Describe the morphology of the red blood cells.
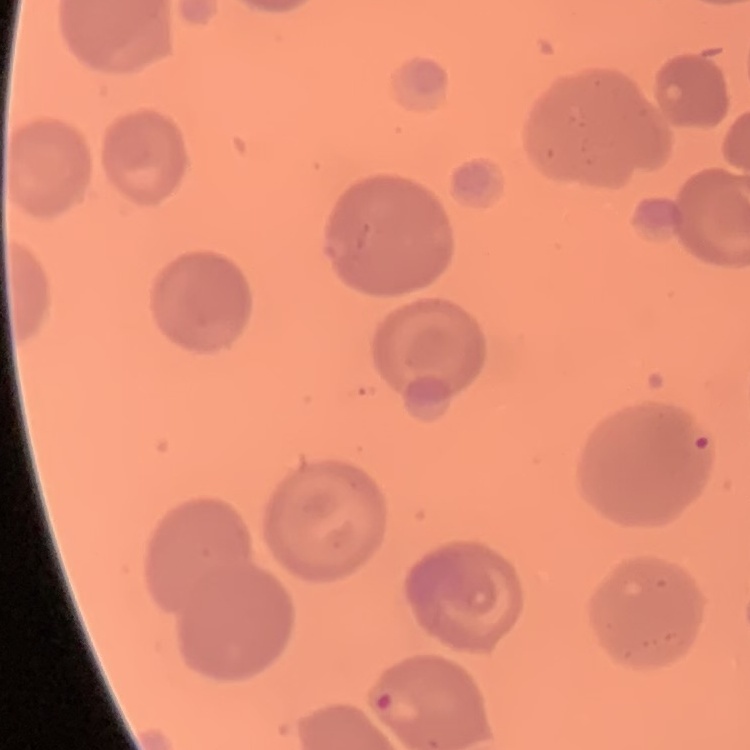
They show no rouleaux formation.

Summary:
  - Preparation: thin blood smear
  - Stain: Field's or Giemsa
  - Image type: square crop of a larger photomicrograph